Report the malaria status of this cell.
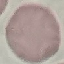

It is uninfected.

Summary:
  - Capture: smartphone camera at the microscope eyepiece
  - Preparation: thin smear
  - Image type: automatically extracted cell patch, resized to 64 × 64 pixels
  - Stain: Giemsa